Outline each blood parasite and name the species.
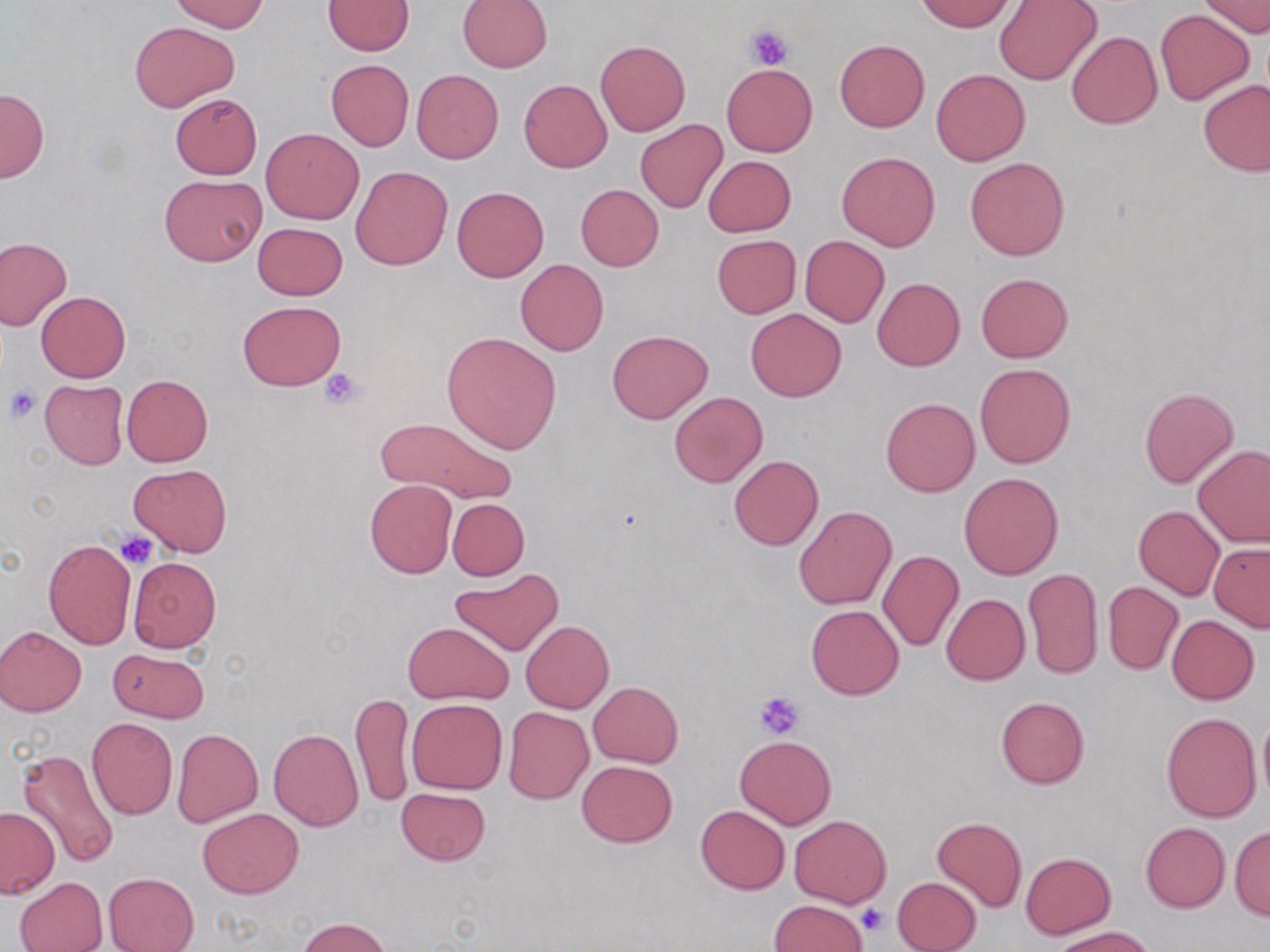
No blood parasites seen.

Approximate bounding boxes as [x1, y1, x2, y2] in pixels. Uninfected red blood cell locations: [172, 0, 268, 33], [458, 0, 552, 71], [1199, 0, 1269, 37], [323, 1, 415, 56], [916, 1, 1014, 32], [994, 1, 1102, 85], [1154, 9, 1256, 105], [130, 20, 239, 112], [1067, 31, 1162, 129], [834, 39, 929, 132], [596, 40, 689, 135], [325, 59, 413, 151], [720, 64, 818, 157], [930, 68, 1030, 166], [411, 69, 503, 164], [519, 79, 613, 173], [1199, 80, 1269, 176], [1, 87, 50, 182], [169, 92, 262, 179], [635, 118, 729, 213], [261, 129, 363, 224], [836, 152, 940, 251], [703, 155, 796, 237], [965, 157, 1069, 260], [351, 166, 452, 270], [159, 174, 266, 265], [575, 184, 663, 271], [452, 186, 550, 282], [252, 222, 347, 299], [712, 235, 801, 318], [800, 236, 889, 327], [0, 237, 72, 331], [515, 259, 607, 356], [975, 273, 1073, 363], [872, 277, 965, 371], [36, 291, 130, 382], [238, 300, 346, 390], [746, 308, 846, 402], [607, 329, 713, 424], [441, 332, 561, 453], [974, 362, 1076, 469], [121, 374, 213, 466], [40, 380, 128, 469], [1138, 388, 1239, 489], [670, 391, 767, 488], [881, 397, 979, 496], [890, 412, 1004, 539], [377, 417, 518, 506], [1192, 444, 1270, 547], [729, 455, 823, 550], [129, 464, 232, 556], [959, 472, 1064, 579], [365, 478, 457, 578], [447, 498, 529, 580], [795, 505, 897, 611], [1133, 505, 1224, 600], [43, 538, 136, 649], [1209, 543, 1270, 631], [876, 550, 964, 654], [128, 557, 221, 651], [450, 567, 562, 657], [1022, 567, 1102, 682], [1102, 581, 1183, 676], [941, 593, 1030, 685], [806, 605, 903, 700], [1166, 616, 1259, 704], [520, 620, 614, 713], [403, 622, 512, 704], [0, 626, 87, 716], [108, 649, 208, 724], [588, 682, 683, 767], [350, 690, 414, 809], [995, 695, 1090, 789], [407, 698, 507, 794], [503, 706, 592, 803], [1162, 711, 1262, 822], [1257, 712, 1269, 809], [87, 716, 178, 819], [172, 728, 263, 828], [269, 729, 363, 830], [735, 735, 836, 829], [18, 749, 122, 872], [577, 759, 678, 848], [396, 788, 490, 865], [695, 806, 789, 895], [0, 807, 58, 899], [197, 808, 302, 898], [790, 814, 890, 907], [931, 816, 1027, 911], [1140, 821, 1230, 911], [1230, 825, 1270, 921], [1020, 851, 1115, 939], [103, 872, 198, 952], [14, 876, 107, 952], [892, 876, 982, 952], [769, 900, 868, 951], [297, 918, 392, 952], [1051, 927, 1160, 952]. Platelet locations: [746, 25, 793, 69], [321, 367, 368, 410], [3, 384, 41, 425], [116, 531, 158, 569], [754, 690, 805, 739], [856, 903, 887, 935]. Slide-level diagnosis: negative for blood parasites. Optical microscopy. May-Grünwald-Giemsa stain. Image is 1270×952 pixels. Captured at 1000x magnification. Single field of view. Thin blood film.